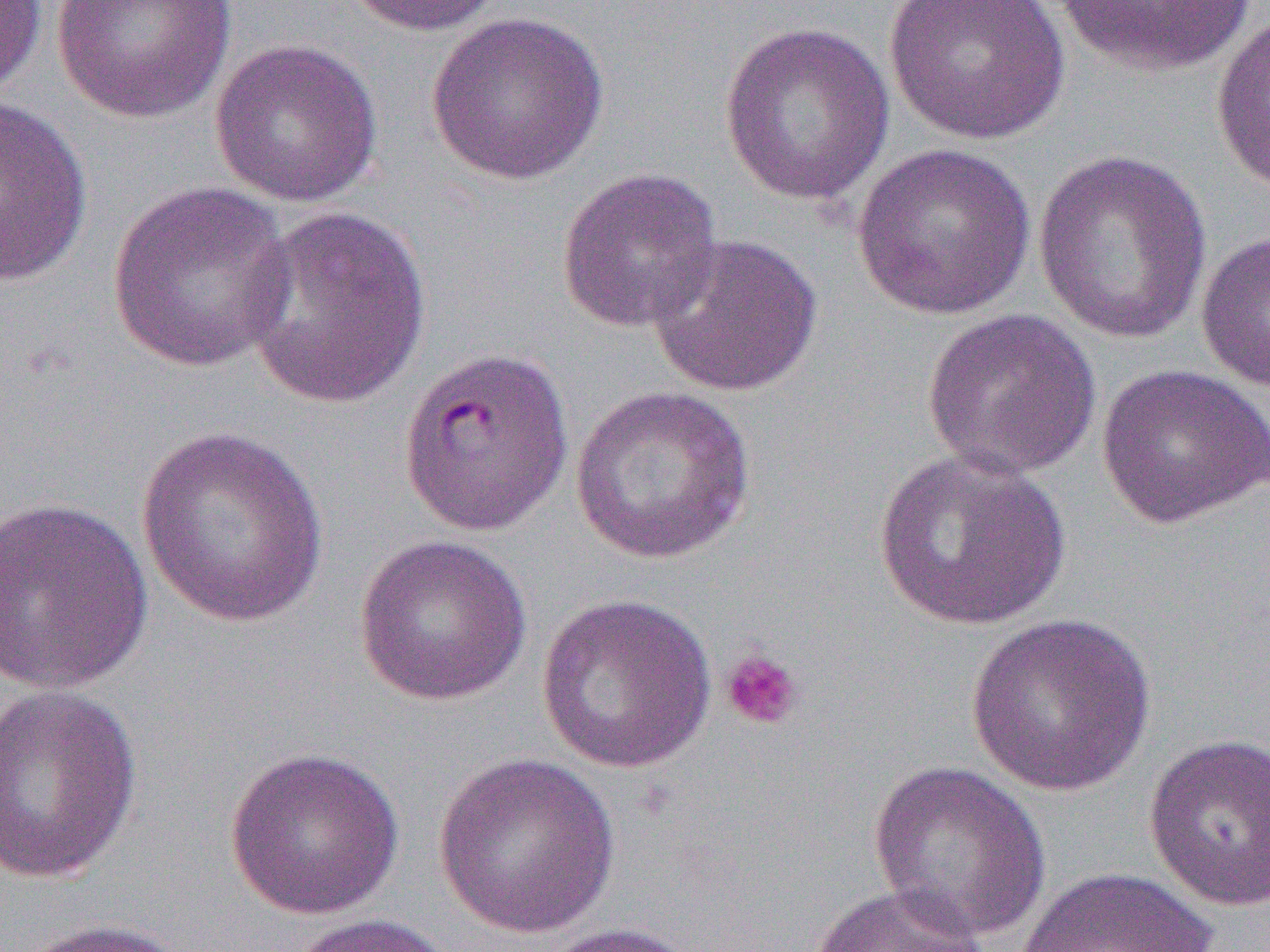

slide-level diagnosis = Plasmodium falciparum
magnification = 1000x
uninfected red blood cell locations = approximate bounding boxes as (x1, y1, x2, y2) in pixels: (0, 0, 48, 101), (50, 0, 238, 123), (337, 0, 508, 37), (883, 0, 1070, 145), (1053, 0, 1257, 77), (1210, 11, 1270, 194), (424, 12, 610, 186), (718, 20, 895, 206), (209, 37, 384, 207), (0, 95, 93, 289), (851, 142, 1037, 321), (1032, 149, 1213, 343), (556, 166, 724, 333), (106, 181, 297, 373), (238, 207, 432, 412), (1196, 230, 1270, 393), (646, 233, 823, 397), (919, 306, 1103, 480), (1095, 363, 1270, 531), (569, 385, 758, 565), (134, 424, 330, 628), (873, 449, 1072, 631), (0, 495, 155, 696), (353, 534, 532, 706), (535, 592, 718, 774), (963, 612, 1156, 798), (1, 682, 144, 887), (1142, 732, 1270, 913), (223, 746, 406, 921), (432, 752, 621, 939), (867, 759, 1051, 942), (1012, 866, 1219, 952), (807, 883, 988, 952), (285, 913, 461, 952), (13, 917, 191, 952), (535, 921, 704, 952)
modality = optical microscopy
image size = 1270×952 pixels
platelet locations = approximate bounding boxes as (x1, y1, x2, y2) in pixels: (719, 649, 806, 731)
field of view = one of a larger specimen
preparation = thin blood film